Report the malaria status of this cell.
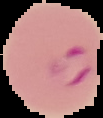
Parasitized.

From a thin blood smear. Image is 103×118 pixels. Segmented cell region on a black background.